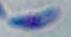

Micrograph. 1000x magnification. Toxoplasma gondii is seen.